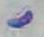 Captured at 1000x magnification. Photomicrograph. Toxoplasma gondii is shown.